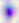

modality: photomicrograph
magnification: 400x
identification: Toxoplasma gondii